Give the position of every leukocyte visible.
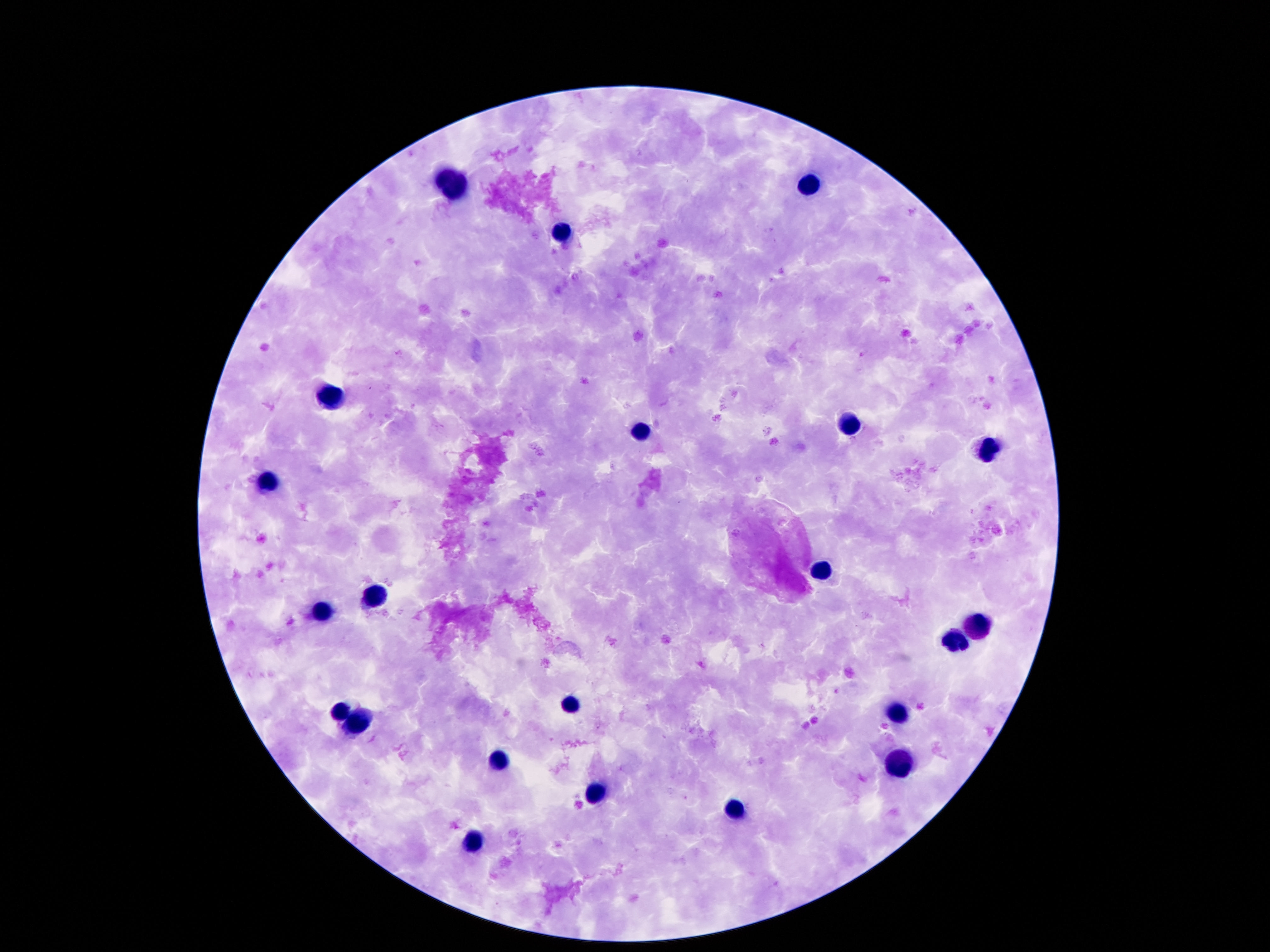
Approximate centers as (x, y) in pixels.
Leukocytes: (451, 182), (812, 184), (564, 233), (329, 396), (847, 426), (642, 431), (984, 447), (270, 482), (822, 566), (375, 597), (322, 612), (982, 624), (956, 642), (570, 704), (341, 713), (898, 715), (356, 722), (499, 762), (904, 767), (595, 793), (732, 809), (472, 842).

patient malaria status = negative
image size = 1270×952 pixels
field of view = one from this slide
magnification = 100x
stain = Giemsa
preparation = thick blood film
capture = smartphone camera through the microscope eyepiece